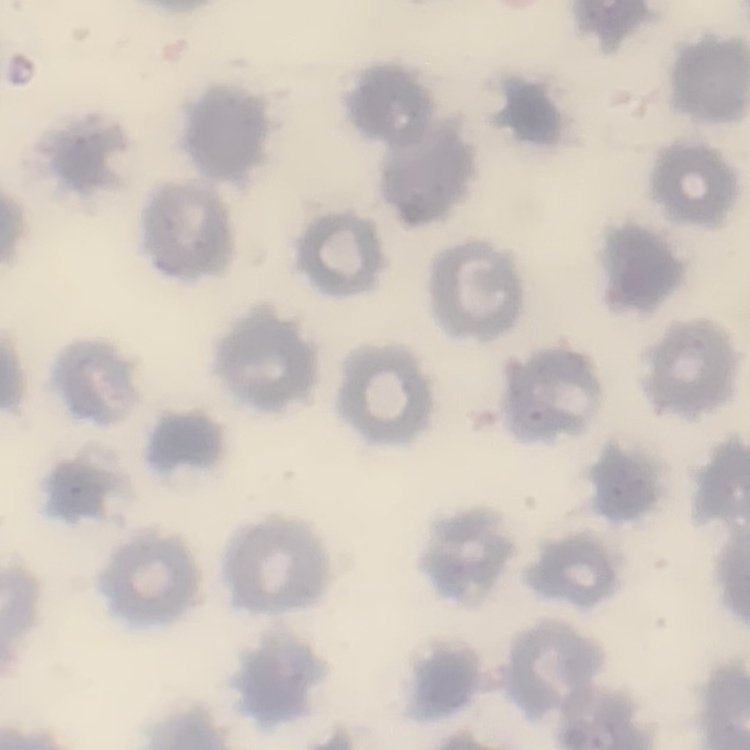

The red blood cells show no rouleaux formation. One tile cut from a larger photomicrograph. Field's or Giemsa stain. Thin blood film.